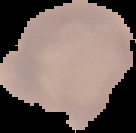

Summary:
  - Result: no malaria parasites seen
  - Preparation: thin blood film
  - Image type: segmented cell region with the area outside set to black
  - Image size: 136×133 pixels